Name the parasite shown.
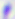

Toxoplasma gondii.

{
  "magnification": "400x",
  "modality": "photomicrograph"
}